Point out each leukocyte.
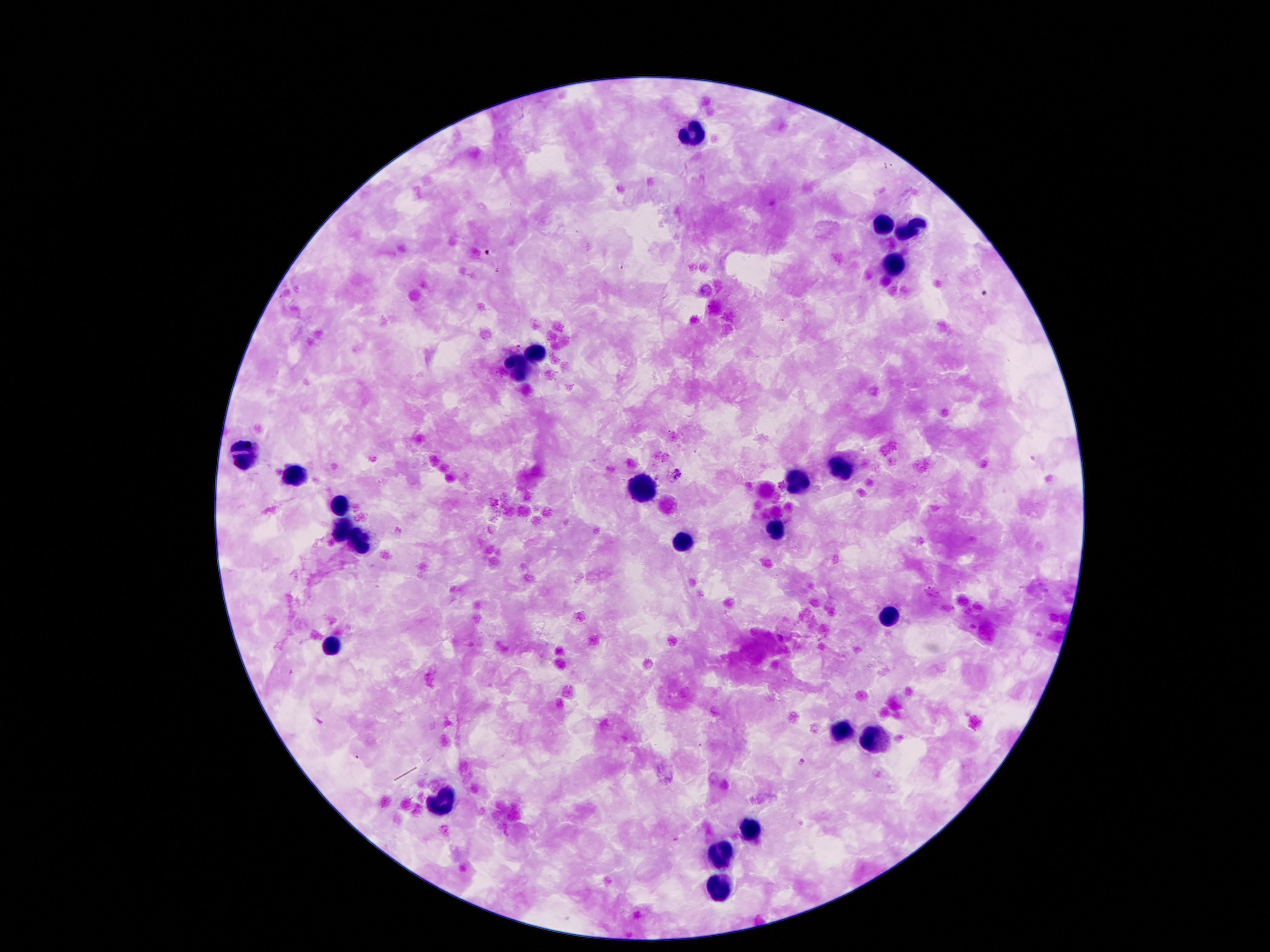

Approximate centers as (x, y) in pixels.
Leukocytes: (691, 135), (884, 223), (909, 228), (895, 266), (539, 350), (519, 366), (244, 455), (841, 466), (291, 475), (798, 482), (641, 489), (344, 502), (773, 527), (339, 532), (355, 543), (682, 543), (889, 618), (332, 641), (840, 732), (876, 738), (440, 802), (751, 827), (724, 854), (719, 886).

{
  "preparation": "thick blood film",
  "stain": "Giemsa",
  "magnification": "100x",
  "field_of_view": "single",
  "image_size": "1270×952 pixels",
  "patient_malaria_status": "infected with Plasmodium falciparum",
  "capture": "smartphone camera through the microscope eyepiece",
  "malaria_parasite_locations": "approximate centers as (x, y) in pixels: (489, 251), (985, 294), (678, 476), (801, 762)"
}